State the preparation type.
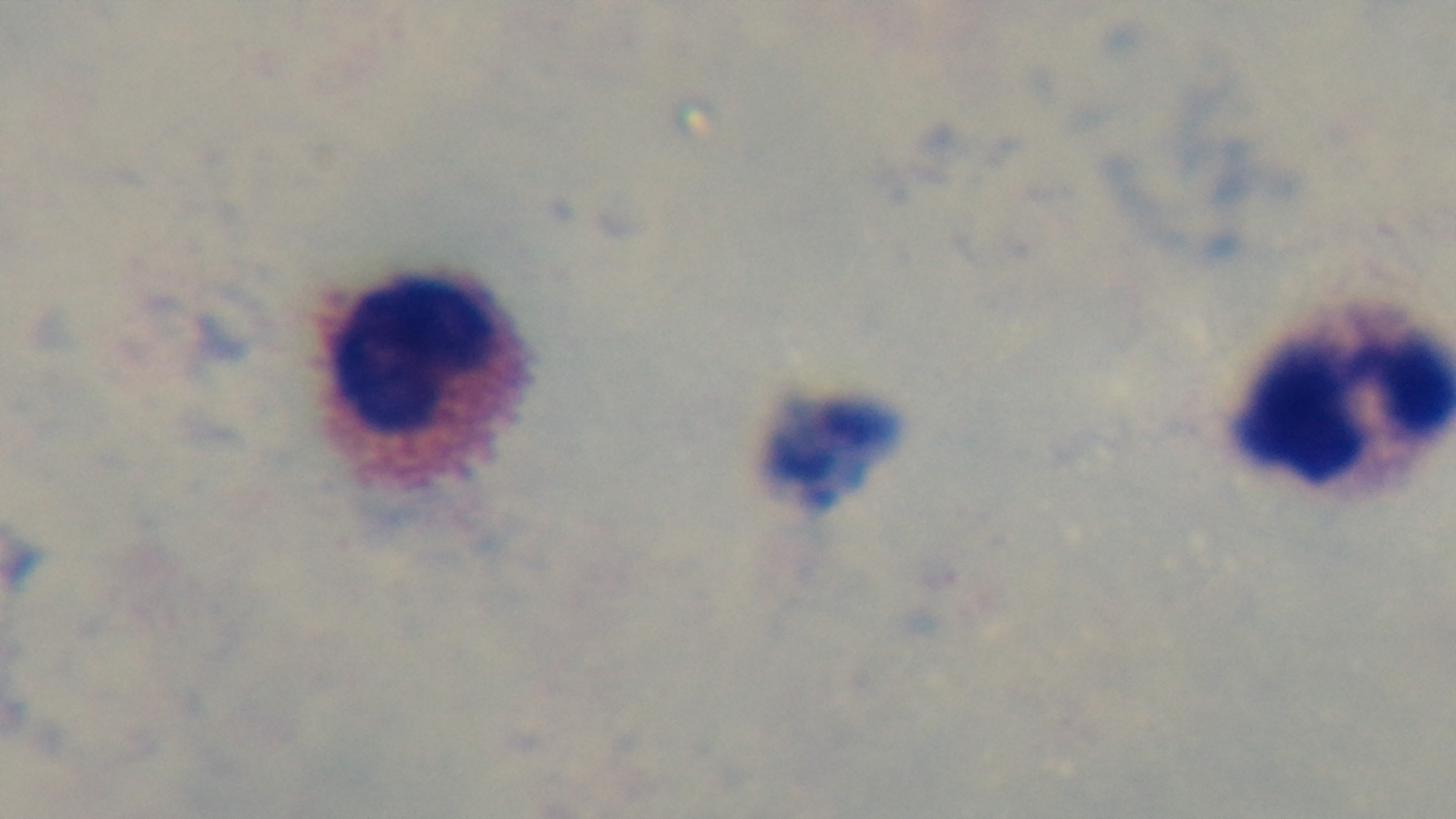
It is a thick blood film.

capture: mounted 4K digital camera
field_of_view: one from the slide
stain: Giemsa
objective: 100x oil immersion
modality: light microscopy
malaria_status: uninfected